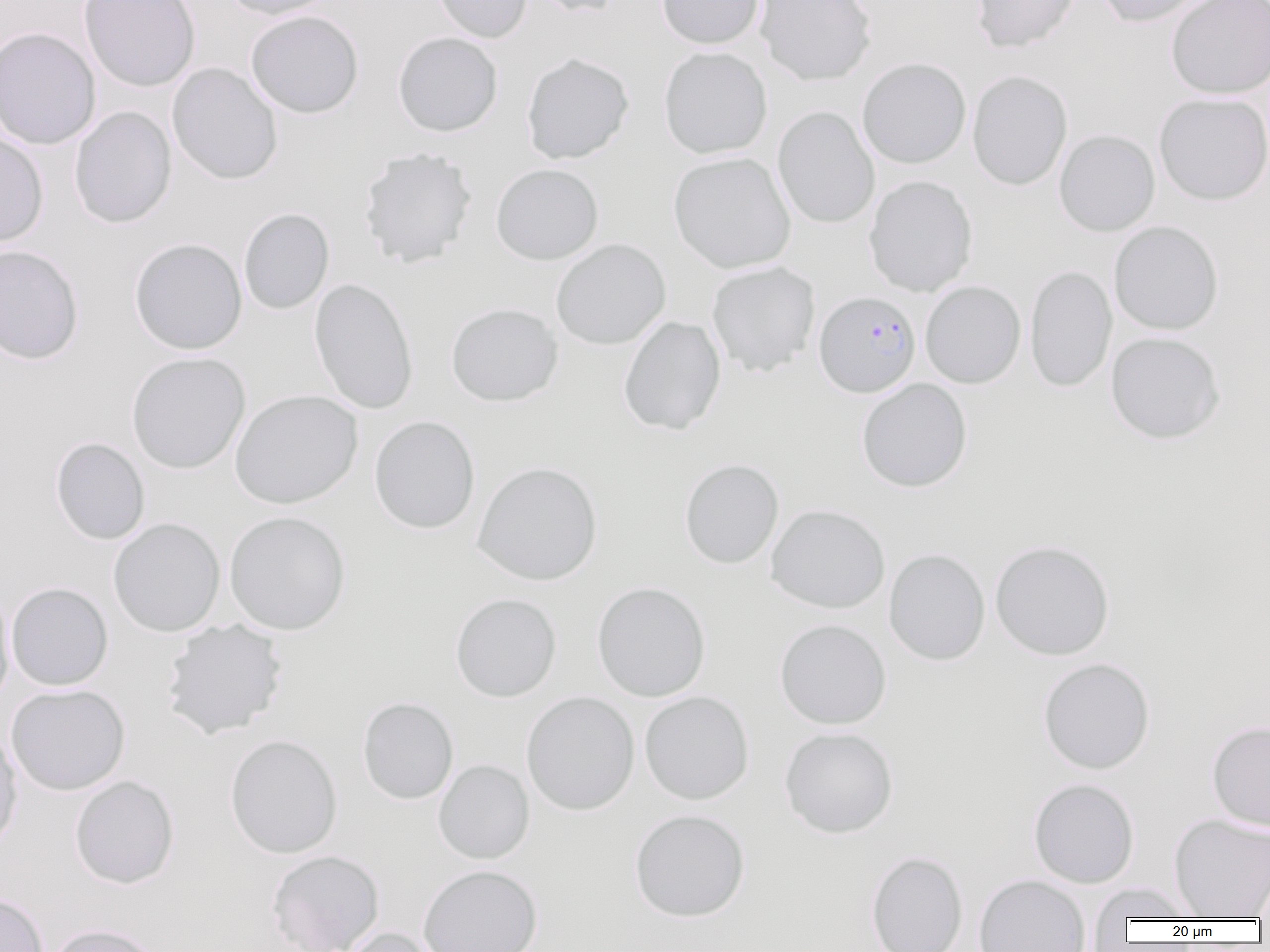

Approximate bounding boxes as (x1,y1)-(x2,y2) corner pairs in pixels. Uninfected red blood cell locations: (79,0)-(200,92), (218,0)-(338,20), (431,0)-(533,43), (532,0)-(627,17), (657,0)-(765,49), (755,0)-(877,86), (970,0)-(1081,53), (1097,0)-(1208,27), (1166,0)-(1270,99), (245,10)-(364,118), (0,27)-(101,151), (393,32)-(503,137), (659,46)-(772,159), (521,52)-(634,164), (857,57)-(971,169), (167,63)-(283,185), (967,70)-(1072,190), (1154,93)-(1270,205), (70,106)-(177,228), (772,106)-(880,229), (1054,129)-(1160,236), (0,132)-(48,248), (358,147)-(478,269), (669,152)-(796,273), (491,163)-(604,265), (864,175)-(978,297), (239,208)-(335,315), (1109,221)-(1223,335), (129,238)-(247,355), (551,239)-(671,350), (0,245)-(84,364), (706,261)-(820,377), (1025,264)-(1117,393), (309,277)-(419,414), (920,280)-(1026,389), (446,303)-(562,407), (618,316)-(726,435), (1105,332)-(1225,444), (126,352)-(251,474), (856,378)-(972,492), (230,389)-(363,509), (369,416)-(480,534), (50,437)-(150,545), (679,458)-(784,569), (472,461)-(603,585), (766,504)-(890,614), (224,510)-(351,635), (108,517)-(226,637), (990,539)-(1115,660), (883,548)-(990,665), (592,581)-(711,702), (6,582)-(113,691), (0,590)-(15,709), (450,592)-(561,702), (160,619)-(288,739), (774,619)-(892,729), (1037,657)-(1155,774), (6,684)-(130,795), (521,691)-(640,815), (639,691)-(754,805), (357,696)-(458,805), (1207,720)-(1270,830), (0,726)-(22,853), (779,727)-(898,838), (225,734)-(343,859), (434,759)-(534,864), (70,775)-(179,889), (1028,778)-(1140,888), (629,809)-(750,922), (1168,814)-(1270,919), (267,849)-(385,952), (865,850)-(968,952), (419,864)-(543,952), (973,874)-(1092,952), (1088,883)-(1200,922), (0,893)-(48,952), (45,923)-(165,952), (339,926)-(447,952). Plasmodium falciparum-infected red blood cell locations: (814,291)-(921,398). Slide-level diagnosis: Plasmodium falciparum. 1000x magnification. Image is 1270×952 pixels. Thin blood smear. One field of a larger specimen. Light microscopy.